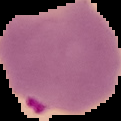

Result: malaria parasites detected. Image is 121×121 pixels. From a thin blood film. The area outside the segmented cell region is set to black.